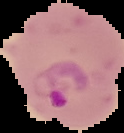
Segmented cell region on a black background. Malaria status: parasitized. From a thin blood smear. Image is 124×133 pixels.